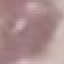

Summary:
  - Result: no malaria parasites seen
  - Stain: Giemsa
  - Image type: cell patch, automatically extracted from a larger field of view and resized to 64 × 64 pixels
  - Capture: smartphone through the microscope eyepiece
  - Preparation: thin smear